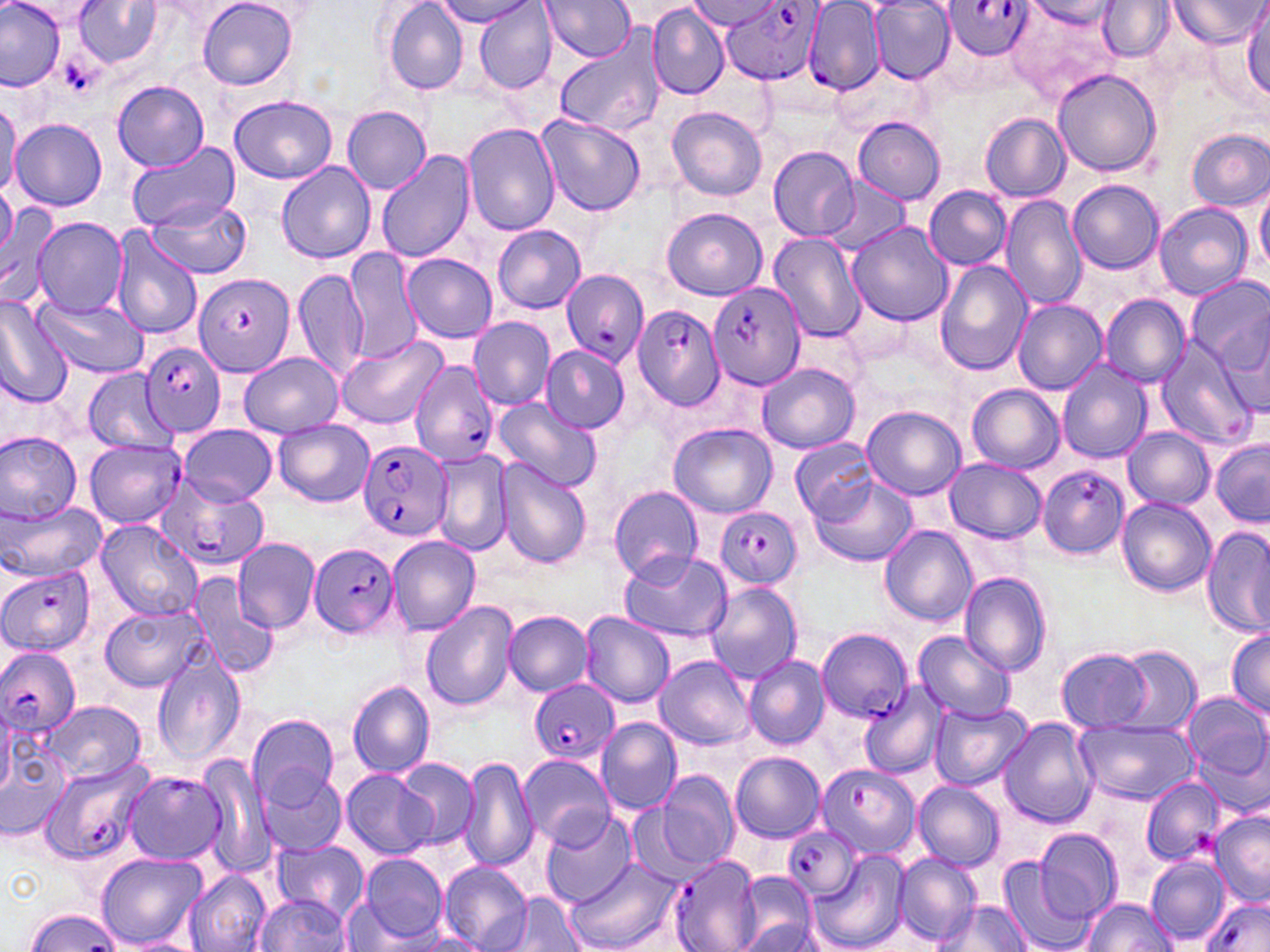

{
  "slide_level_diagnosis": "Plasmodium falciparum",
  "modality": "light microscopy",
  "image_size": "1270×952 pixels",
  "platelet_locations": "approximate bounding boxes as [x1, y1, x2, y2] in pixels: [1195, 827, 1231, 857]",
  "magnification": "1000x",
  "field_of_view": "one of a larger specimen",
  "plasmodium_falciparum_infected_red_blood_cell_locations": "approximate bounding boxes as [x1, y1, x2, y2] in pixels: [940, 0, 1034, 60], [720, 1, 827, 87], [804, 3, 884, 93], [562, 268, 651, 369], [195, 274, 296, 377], [706, 281, 806, 391], [632, 304, 724, 410], [142, 342, 228, 438], [410, 359, 499, 466], [84, 438, 185, 528], [357, 439, 452, 541], [1037, 463, 1131, 560], [156, 479, 267, 571], [715, 507, 803, 588], [309, 544, 401, 639], [1, 565, 98, 658], [816, 626, 912, 722], [0, 647, 82, 737], [529, 681, 619, 763], [37, 754, 156, 867], [818, 763, 920, 856], [123, 770, 227, 866], [784, 825, 860, 902], [669, 855, 763, 952], [1201, 897, 1270, 952]",
  "preparation": "thin blood film",
  "uninfected_red_blood_cell_locations": "approximate bounding boxes as [x1, y1, x2, y2] in pixels: [0, 0, 66, 89], [198, 0, 297, 89], [383, 0, 468, 96], [438, 0, 535, 28], [1168, 0, 1269, 49], [75, 1, 163, 67], [475, 1, 557, 95], [541, 1, 635, 62], [692, 1, 776, 30], [868, 1, 955, 83], [1026, 1, 1121, 28], [1097, 1, 1175, 60], [1007, 4, 1120, 99], [1243, 6, 1270, 101], [647, 7, 729, 99], [553, 28, 667, 137], [836, 62, 930, 140], [1052, 68, 1161, 175], [114, 80, 210, 170], [230, 95, 338, 183], [0, 98, 20, 202], [343, 106, 430, 194], [667, 107, 768, 202], [979, 113, 1071, 202], [536, 114, 646, 216], [852, 116, 945, 204], [12, 118, 107, 212], [462, 123, 560, 236], [1187, 129, 1269, 212], [125, 142, 240, 233], [769, 146, 858, 240], [375, 150, 475, 263], [278, 161, 376, 264], [818, 177, 906, 252], [1069, 180, 1165, 275], [1255, 180, 1270, 276], [0, 181, 18, 257], [923, 185, 1011, 268], [1000, 195, 1087, 310], [146, 197, 250, 280], [1153, 202, 1253, 299], [0, 207, 64, 309], [661, 207, 767, 300], [31, 216, 128, 317], [846, 221, 953, 327], [493, 224, 586, 313], [111, 227, 203, 341], [769, 235, 865, 346], [346, 247, 422, 364], [402, 252, 498, 343], [933, 260, 1032, 377], [293, 268, 367, 382], [1186, 274, 1270, 385], [1100, 295, 1191, 388], [38, 297, 149, 377], [1012, 298, 1106, 394], [0, 299, 71, 409], [468, 317, 555, 409], [338, 334, 448, 430], [1155, 339, 1259, 449], [540, 344, 630, 432], [238, 351, 345, 437], [1056, 360, 1152, 465], [757, 363, 861, 453], [80, 366, 172, 452], [969, 384, 1064, 473], [490, 398, 602, 490], [863, 405, 966, 500], [273, 420, 375, 507], [179, 423, 276, 506], [669, 423, 776, 517], [1123, 427, 1214, 510], [1, 429, 84, 523], [1211, 438, 1270, 528], [791, 440, 879, 521], [432, 448, 513, 555], [946, 458, 1046, 543], [496, 460, 592, 567], [807, 473, 917, 568], [609, 485, 704, 581], [1117, 497, 1216, 596], [2, 502, 108, 581], [95, 520, 202, 621], [880, 525, 976, 627], [1202, 525, 1268, 639], [388, 536, 481, 635], [231, 537, 319, 633], [617, 548, 732, 643], [396, 556, 498, 678], [185, 570, 279, 678], [959, 571, 1053, 677], [707, 581, 802, 683], [420, 600, 518, 711], [101, 604, 206, 692], [504, 611, 592, 696], [580, 612, 674, 706], [1227, 626, 1270, 717], [912, 629, 1015, 723], [1109, 644, 1201, 735], [1057, 647, 1151, 732], [152, 650, 245, 766], [743, 654, 830, 750], [656, 655, 753, 751], [346, 681, 436, 779], [860, 683, 946, 780], [1182, 690, 1269, 796], [42, 699, 147, 784], [928, 701, 1031, 791], [246, 713, 339, 807], [597, 716, 683, 814], [997, 717, 1098, 829], [1070, 719, 1199, 803], [0, 732, 72, 838], [195, 752, 273, 877], [730, 752, 825, 842], [519, 754, 615, 847], [458, 756, 538, 871], [397, 758, 478, 849], [258, 768, 346, 856], [658, 769, 738, 868], [341, 770, 434, 861], [1142, 778, 1229, 868], [913, 779, 1005, 871], [1209, 810, 1269, 907], [540, 812, 638, 908], [1034, 828, 1122, 924], [271, 840, 369, 920], [809, 849, 912, 952], [95, 852, 208, 948], [891, 852, 981, 946], [359, 854, 448, 943], [1145, 855, 1229, 944], [567, 858, 680, 952], [995, 860, 1095, 952], [439, 861, 532, 952], [184, 870, 271, 952], [732, 873, 820, 952], [507, 890, 585, 952], [254, 893, 350, 950], [339, 896, 411, 951], [1078, 897, 1178, 951], [932, 899, 1029, 951], [415, 933, 487, 951], [129, 938, 196, 952]",
  "stain": "May-Grünwald-Giemsa"
}